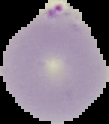

image_type: segmented cell region on a black background
image_size: 109×124 pixels
result: Plasmodium parasites identified
preparation: thin blood film